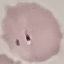

result: negative for malaria parasites
preparation: thin blood film
stain: Giemsa
capture: smartphone camera at the microscope eyepiece
image_type: automatically extracted cell patch, resized to 64 × 64 pixels